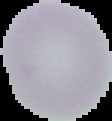
malaria status = uninfected
preparation = thin blood smear
image type = segmented cell region on a black background
image size = 112×121 pixels